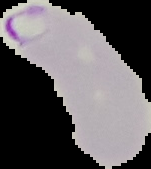

Result: malaria parasites detected. The area outside the segmented cell region is set to black. Image is 151×169 pixels. From a thin blood smear.